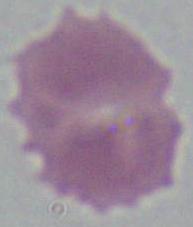
identification = red blood cell
modality = micrograph
magnification = 1000x